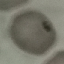

malaria status = uninfected
preparation = thin blood film
capture = smartphone through the microscope eyepiece
stain = Giemsa
image type = cell patch, automatically extracted from a larger field of view and resized to 64 × 64 pixels